State which parasite is depicted.
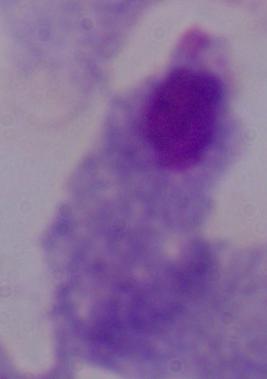
A trichomonad.

modality = photomicrograph
magnification = 1000x